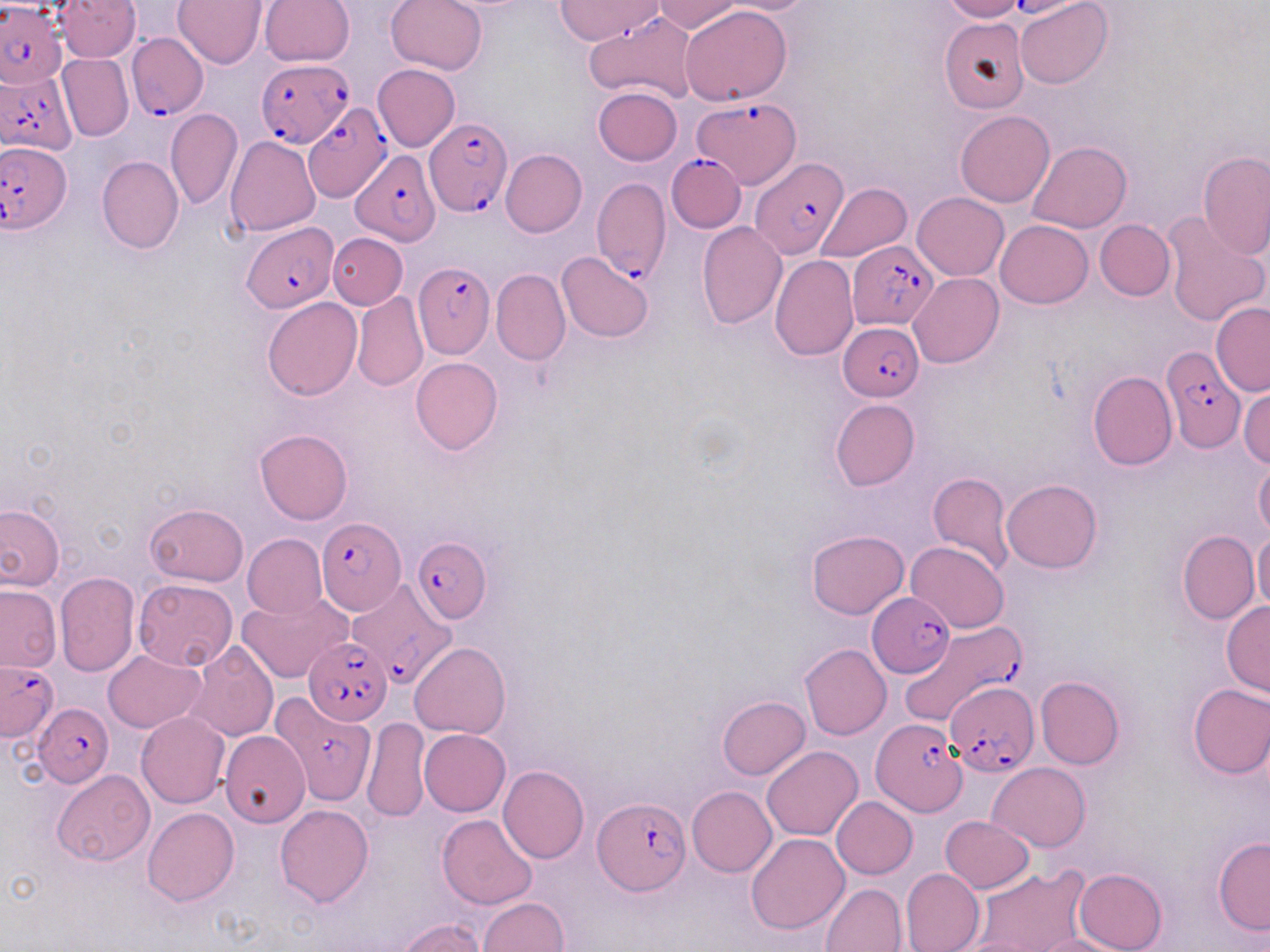

{
  "slide_level_diagnosis": "Plasmodium falciparum",
  "field_of_view": "one of a larger specimen",
  "preparation": "thin blood smear",
  "uninfected_red_blood_cell_locations": "approximate bounding boxes as (x1,y1)-(x2,y2) corner pairs in pixels: (56,0)-(140,61), (173,0)-(266,69), (260,0)-(354,67), (386,0)-(488,75), (554,0)-(663,44), (653,0)-(743,34), (716,0)-(818,14), (1016,0)-(1112,89), (938,1)-(1027,22), (679,6)-(792,105), (939,16)-(1031,115), (57,54)-(133,142), (373,63)-(460,152), (593,86)-(682,165), (165,109)-(242,210), (955,110)-(1054,208), (227,136)-(320,236), (1027,141)-(1131,232), (501,149)-(587,238), (1198,151)-(1270,259), (97,156)-(184,254), (816,183)-(912,263), (912,192)-(1008,280), (1161,211)-(1269,327), (996,219)-(1092,309), (1095,219)-(1175,301), (695,221)-(788,330), (328,233)-(408,310), (557,250)-(654,343), (770,255)-(859,359), (492,269)-(570,365), (909,272)-(1004,369), (353,290)-(429,391), (262,296)-(363,401), (1211,301)-(1270,396), (410,357)-(503,455), (1087,372)-(1176,470), (1239,387)-(1270,467), (830,398)-(920,491), (254,428)-(353,524), (1254,455)-(1270,539), (927,471)-(1013,574), (1002,479)-(1100,573), (0,503)-(64,591), (145,503)-(249,586), (806,528)-(909,620), (1177,529)-(1259,625), (1253,530)-(1270,614), (243,533)-(327,620), (906,540)-(1010,633), (54,571)-(140,676), (133,578)-(237,671), (0,584)-(62,672), (237,593)-(350,684), (1221,600)-(1270,697), (186,642)-(279,743), (410,643)-(510,739), (799,644)-(892,740), (102,650)-(205,733), (1036,676)-(1125,769), (1187,683)-(1270,778), (717,695)-(810,780), (136,710)-(230,808), (362,717)-(432,821), (418,729)-(510,816), (220,730)-(310,828), (762,746)-(863,840), (988,762)-(1091,851), (498,766)-(588,863), (52,769)-(154,866), (688,786)-(777,877), (832,797)-(918,878), (274,804)-(374,907), (141,807)-(239,905), (437,814)-(537,909), (941,816)-(1034,893), (746,832)-(850,934), (1213,837)-(1270,934), (974,866)-(1090,952), (1072,867)-(1167,952), (901,868)-(984,952), (820,883)-(907,952), (476,897)-(569,952), (400,917)-(488,952), (1029,933)-(1134,952)",
  "image_size": "1270×952 pixels",
  "stain": "May-Grünwald-Giemsa",
  "magnification": "1000x",
  "plasmodium_falciparum_infected_red_blood_cell_locations": "approximate bounding boxes as (x1,y1)-(x2,y2) corner pairs in pixels: (0,1)-(68,87), (125,33)-(208,119), (260,62)-(356,148), (0,66)-(77,154), (304,103)-(391,201), (425,119)-(510,214), (2,141)-(70,231), (349,150)-(441,248), (666,152)-(747,232), (752,158)-(850,259), (591,176)-(670,283), (240,222)-(339,312), (849,243)-(939,329), (413,261)-(494,357), (840,325)-(923,399), (1160,347)-(1246,451), (317,518)-(405,614), (412,537)-(492,624), (350,577)-(453,683), (867,591)-(955,677), (908,619)-(1026,740), (304,636)-(393,724), (0,661)-(58,741), (945,682)-(1039,775), (277,688)-(382,799), (31,704)-(111,787), (871,721)-(969,819), (593,797)-(690,894)",
  "modality": "light microscopy"
}